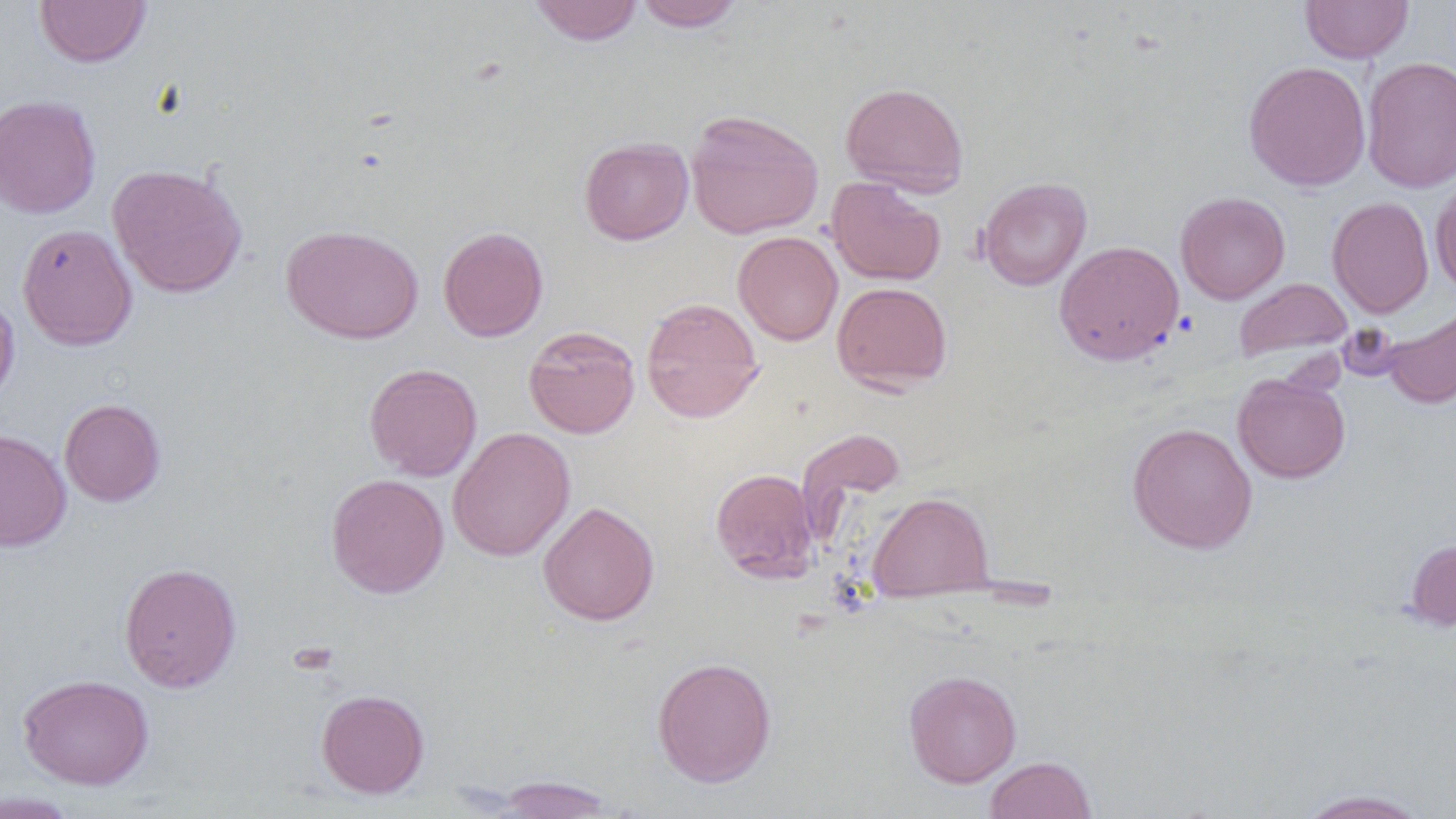
Approximate bounding boxes as [x1, y1, x2, y2] in pixels. Uninfected red blood cell locations: [34, 0, 152, 68], [528, 0, 644, 45], [633, 0, 745, 31], [1300, 0, 1413, 63], [1361, 56, 1456, 193], [1243, 60, 1371, 191], [840, 81, 969, 196], [0, 94, 102, 219], [685, 109, 824, 239], [579, 136, 694, 245], [106, 163, 248, 298], [826, 176, 946, 286], [977, 176, 1092, 291], [1430, 177, 1456, 296], [1175, 191, 1290, 304], [1327, 196, 1434, 318], [17, 223, 137, 350], [280, 224, 424, 344], [438, 226, 549, 342], [732, 231, 843, 346], [1054, 240, 1184, 365], [1234, 277, 1352, 361], [831, 281, 953, 392], [0, 292, 20, 408], [640, 297, 764, 423], [1381, 305, 1456, 410], [523, 325, 641, 438], [364, 362, 483, 481], [1232, 372, 1350, 483], [58, 398, 166, 507], [1127, 422, 1258, 554], [796, 426, 907, 531], [448, 427, 575, 562], [0, 428, 72, 552], [710, 468, 819, 583], [325, 473, 450, 599], [867, 491, 994, 600], [537, 501, 660, 626], [1404, 537, 1456, 632], [119, 561, 242, 692], [651, 657, 777, 787], [904, 669, 1022, 787], [18, 673, 154, 790], [315, 689, 430, 798], [984, 755, 1097, 819], [489, 775, 618, 818], [1294, 788, 1432, 818], [0, 791, 81, 818]. Slide-level diagnosis: no evidence of blood parasites. Light microscopy. 1000x magnification. Thin blood film. Image is 1456×819 pixels. One field of a larger specimen.